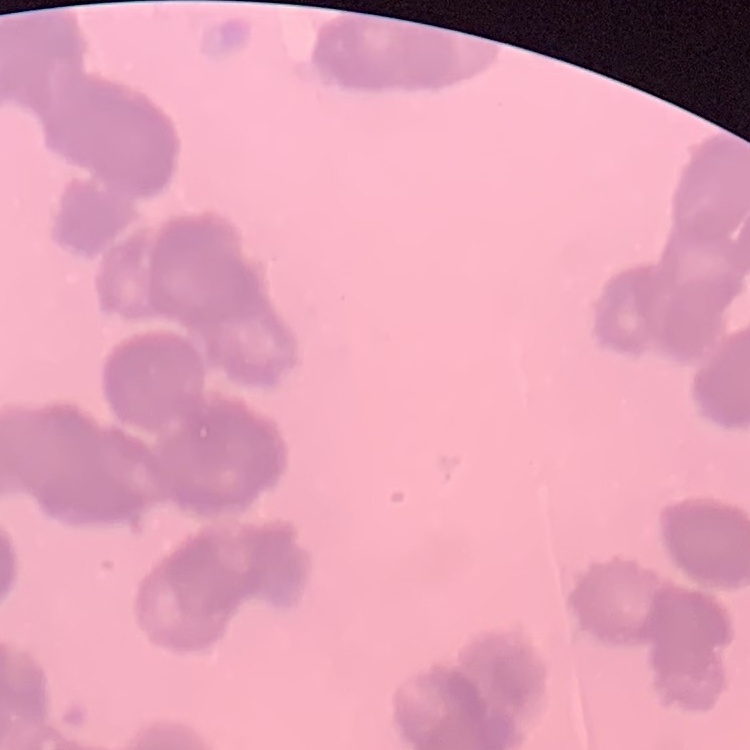
erythrocyte morphology = rouleaux formation
image type = square crop of a larger photomicrograph
stain = Field's or Giemsa
preparation = thin blood film